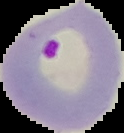

Summary:
  - Image type: segmented cell region on a black background
  - Preparation: thin blood smear
  - Malaria status: parasitized
  - Image size: 124×133 pixels